Point out leukocytes.
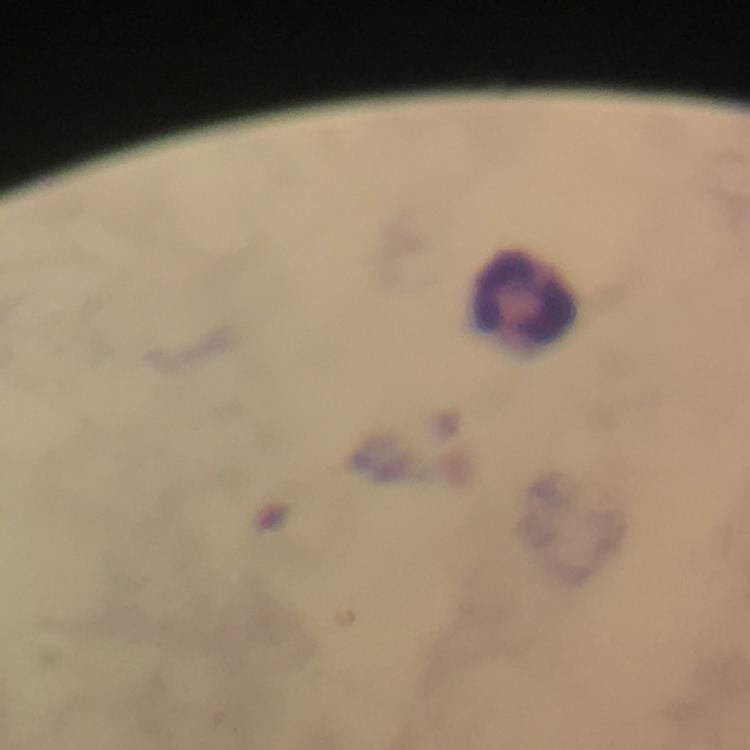

Approximate centers as {x, y} in pixels.
Leukocytes: {526, 300}.

Immersion oil applied. Giemsa-stained preparation. Image is 750×750 pixels. Photographed with a smartphone mounted on the microscope. Malaria parasites: none detected. A crop from one field of view. 100x magnification. Thick smear. From a malaria diagnostic workup.